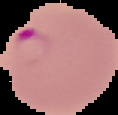 Cell region segmented out of the field of view; the surrounding area is masked to black. Result: Plasmodium parasites detected. From a thin blood film. Image is 118×115 pixels.